Identify the preparation type.
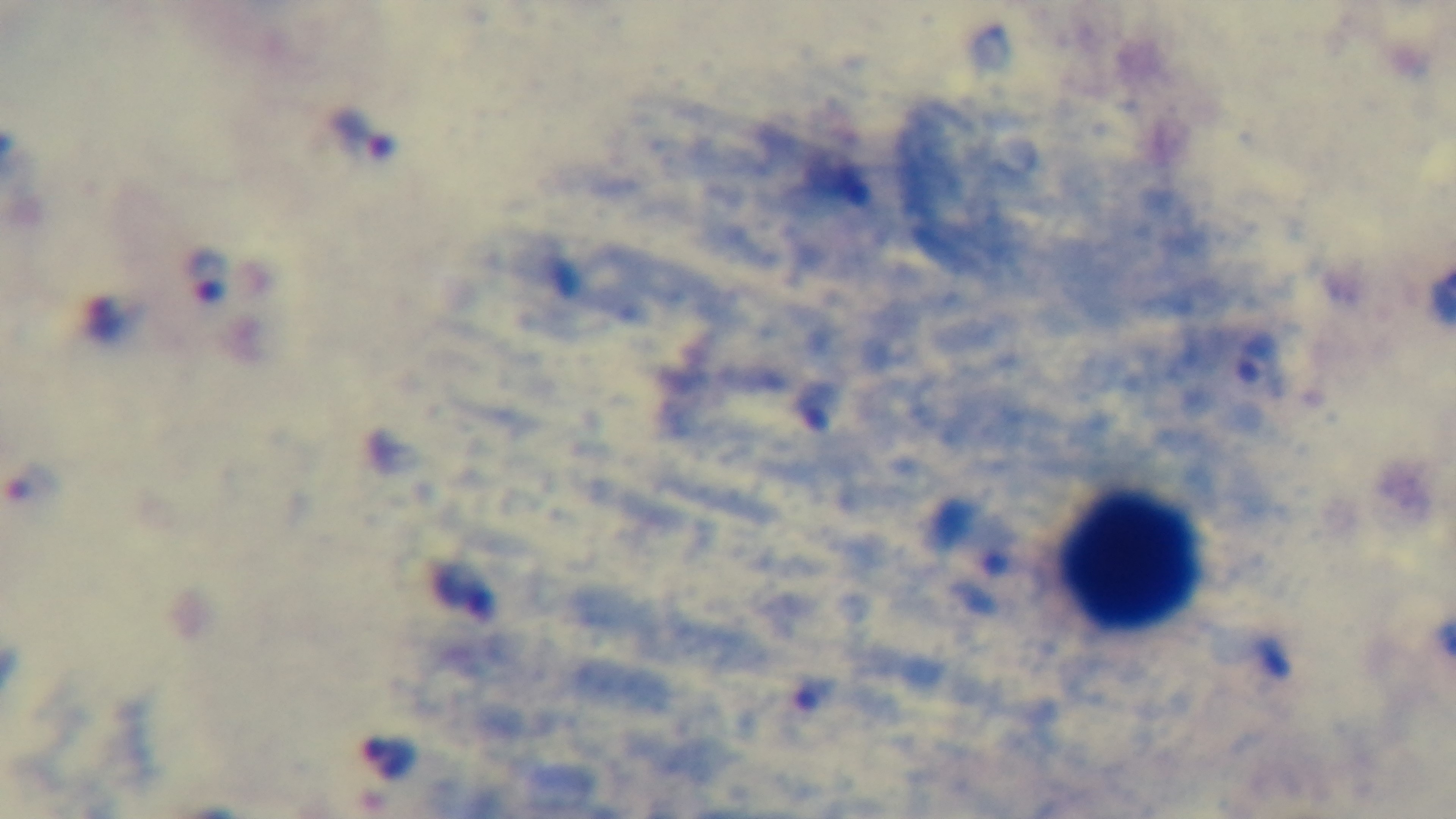
A thick smear.

field of view = single
stain = Giemsa
objective = 100x oil immersion
capture = mounted 4K digital camera
malaria status = positive
modality = light microscopy